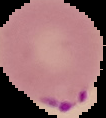
image_size: 106×118 pixels
image_type: cell region segmented out of the field of view; surrounding area masked to black
preparation: thin blood film
result: Plasmodium parasites identified